Give the extent of all Plasmodium falciparum-infected red blood cells.
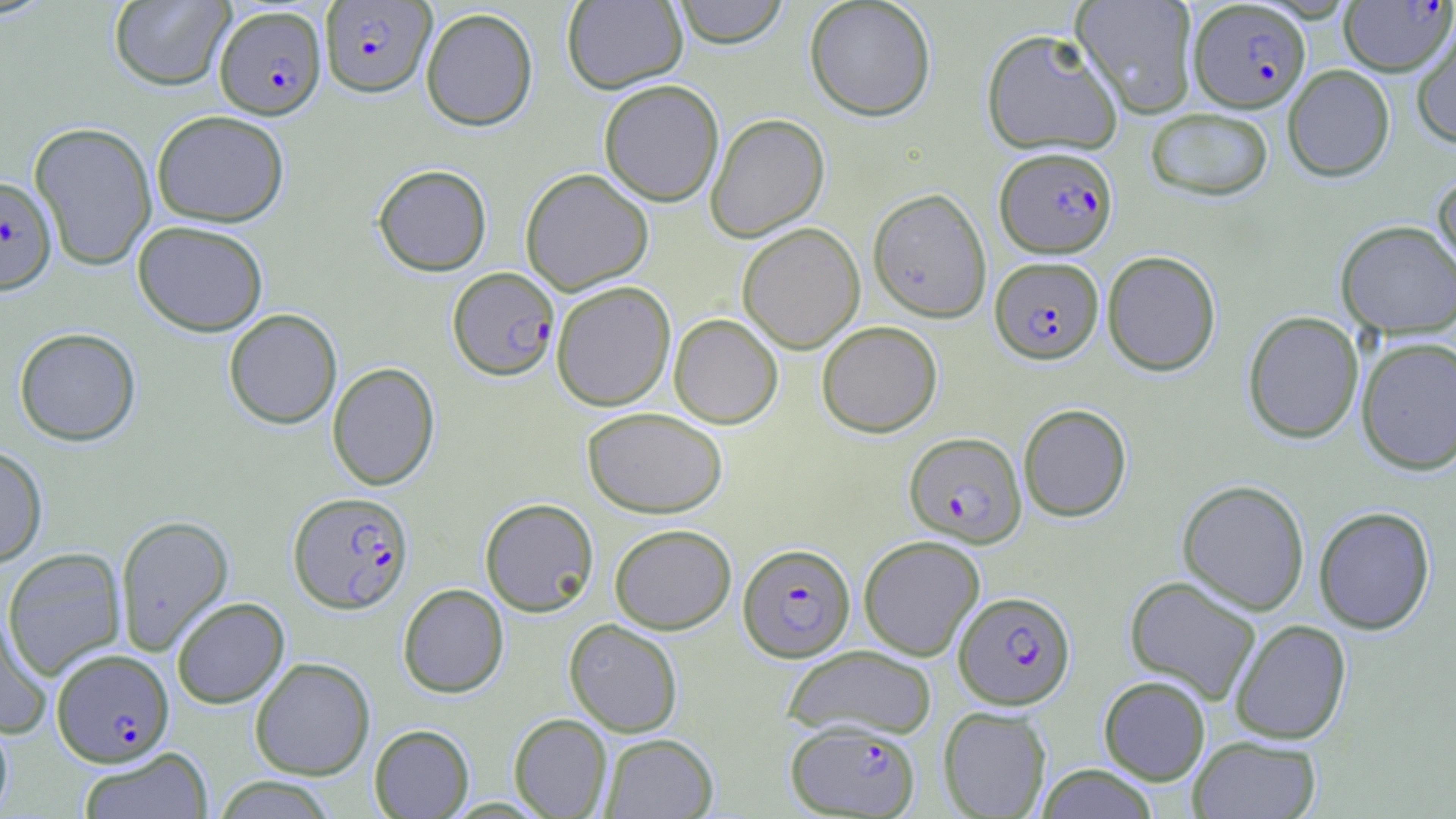

Approximate bounding boxes as (x1,y1)-(x2,y2) corner pairs in pixels.
Plasmodium falciparum-infected red blood cells: (1339,0)-(1456,76), (320,1)-(435,97), (1189,1)-(1310,113), (214,6)-(327,119), (995,146)-(1118,258), (0,175)-(57,294), (990,257)-(1103,364), (448,267)-(559,380), (904,431)-(1026,547), (288,491)-(414,614), (738,543)-(855,661), (954,590)-(1075,709), (52,648)-(174,766), (786,720)-(920,817).

Summary:
  - Uninfected red blood cell locations: (562,0)-(688,93), (672,0)-(789,47), (804,0)-(936,120), (1071,0)-(1199,118), (108,1)-(235,90), (420,7)-(538,131), (1411,21)-(1456,148), (981,28)-(1123,157), (1282,64)-(1395,181), (599,79)-(724,206), (1144,107)-(1274,201), (152,109)-(289,227), (705,113)-(830,242), (29,121)-(157,270), (372,164)-(492,276), (520,168)-(654,295), (1431,168)-(1456,282), (867,187)-(992,322), (133,220)-(268,337), (1336,220)-(1456,339), (737,222)-(865,354), (1102,250)-(1221,376), (551,281)-(676,411), (224,309)-(342,429), (1243,310)-(1364,443), (669,313)-(783,428), (816,321)-(942,437), (14,326)-(141,446), (1355,336)-(1456,474), (327,361)-(440,490), (1018,403)-(1132,522), (582,406)-(727,518), (0,445)-(48,567), (1177,479)-(1310,614), (479,498)-(599,617), (1313,506)-(1436,635), (115,515)-(234,656), (610,524)-(736,634), (858,535)-(985,661), (2,547)-(127,680), (1124,575)-(1262,703), (398,583)-(509,698), (171,597)-(290,708), (0,606)-(52,740), (564,618)-(683,737), (1230,619)-(1351,744), (782,645)-(937,739), (250,657)-(375,780), (1099,675)-(1210,785), (938,706)-(1052,818), (0,712)-(14,817), (509,713)-(612,818), (369,724)-(474,818), (601,733)-(718,818), (1188,735)-(1321,818), (78,747)-(213,819), (1035,764)-(1159,818), (211,776)-(340,818)
  - Slide-level diagnosis: Plasmodium falciparum
  - Preparation: thin blood film
  - Magnification: 1000x
  - Stain: May-Grünwald-Giemsa
  - Image size: 1456×819 pixels
  - Modality: optical microscopy
  - Field of view: single